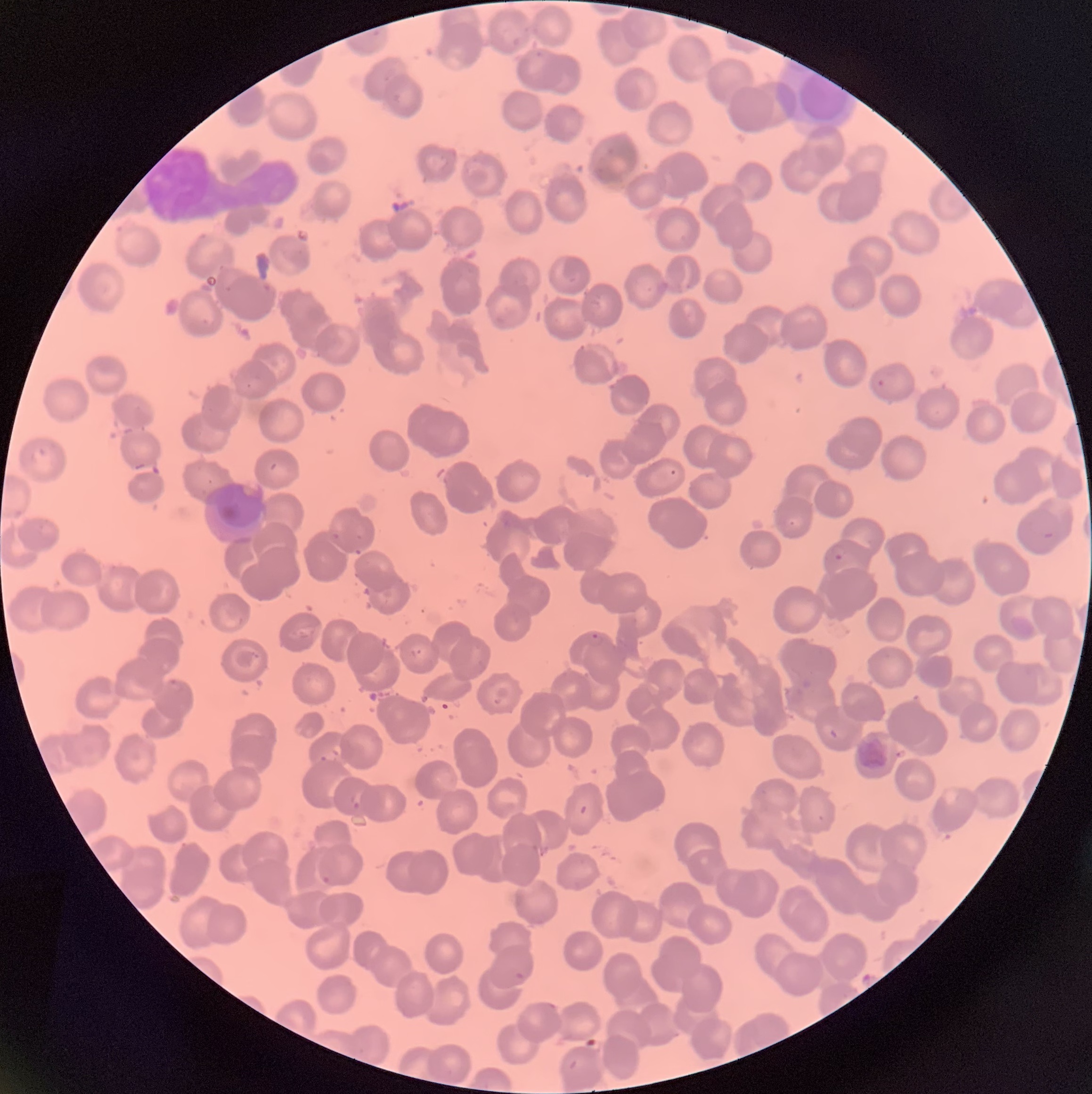

Summary:
  - Coordinate format: approximate bounding boxes as [x1, y1, x2, y2] in pixels
  - Plasmodium parasite locations: [874, 371, 895, 390], [829, 542, 847, 561], [587, 632, 604, 648], [409, 645, 427, 661], [168, 678, 185, 692], [320, 748, 340, 764], [349, 788, 363, 808], [321, 875, 332, 885], [514, 972, 530, 982], [546, 1001, 557, 1010]
  - Image size: 1092×1094 pixels
  - Red blood cell morphology: rouleaux formation
  - Preparation: thin blood film
  - Modality: light microscopy